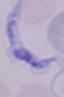
Summary:
  - Modality: photomicrograph
  - Identification: trypanosome
  - Magnification: 1000x